Comment on the morphology of the red blood cells.
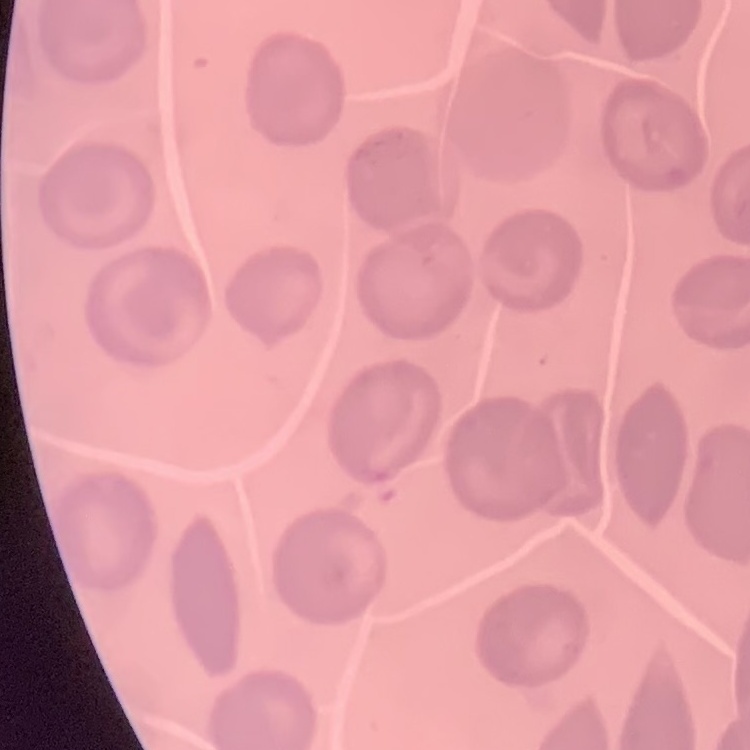

They show no rouleaux formation.

Summary:
  - Image type: square crop of a larger photomicrograph
  - Stain: Field's or Giemsa
  - Preparation: thin blood film